Assess the morphology of the erythrocytes.
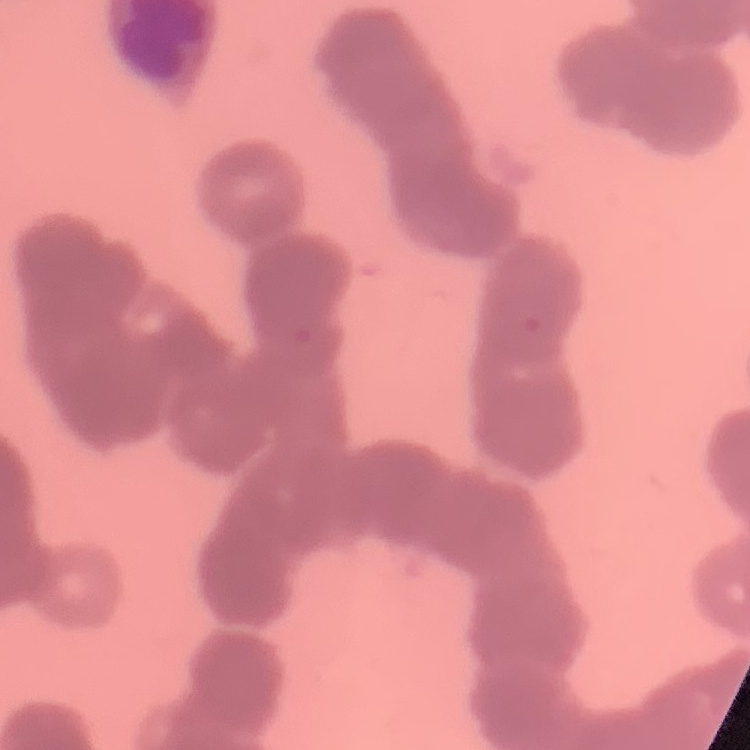

They show rouleaux formation.

preparation = thin peripheral smear
image type = square crop of a larger photomicrograph
stain = Field's or Giemsa